Comment on the morphology of the erythrocytes.
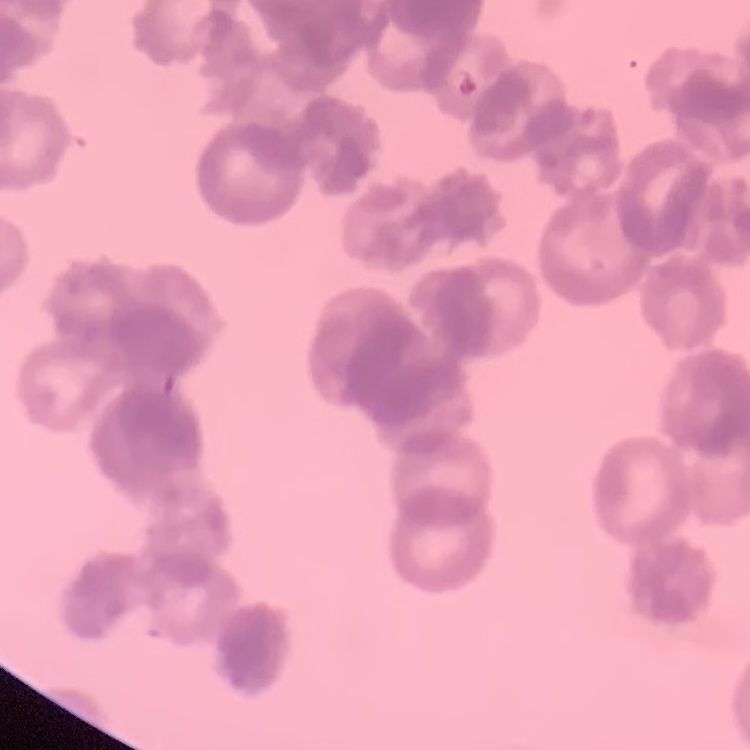

They show rouleaux formation.

Summary:
  - Stain: Field's or Giemsa
  - Image type: square crop of a larger photomicrograph
  - Preparation: thin blood smear